Assess this cell for malaria.
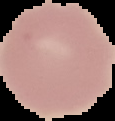

Uninfected.

Summary:
  - Image size: 115×121 pixels
  - Preparation: thin blood film
  - Image type: cell region segmented out of the field of view; surrounding area masked to black